Assess the morphology of the red blood cells.
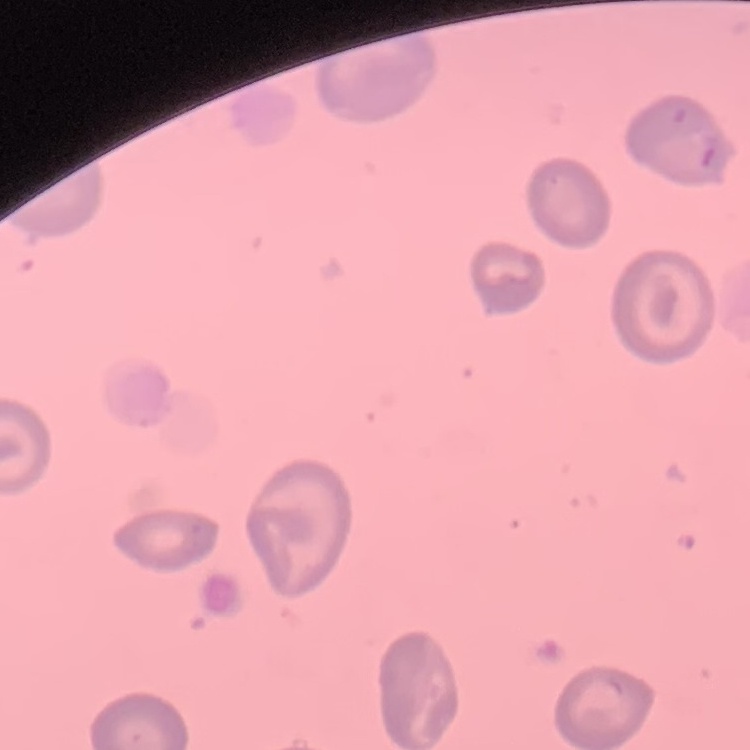

They show no rouleaux formation.

Thin peripheral smear. Stained with either Field's or Giemsa. Square crop of a larger photomicrograph.